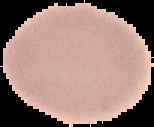
Summary:
  - Image size: 154×127 pixels
  - Preparation: thin blood film
  - Result: negative for malaria parasites
  - Image type: segmented cell region on a black background